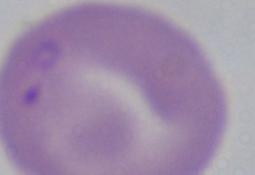 A Babesia parasite is seen. 1000x magnification. Micrograph.